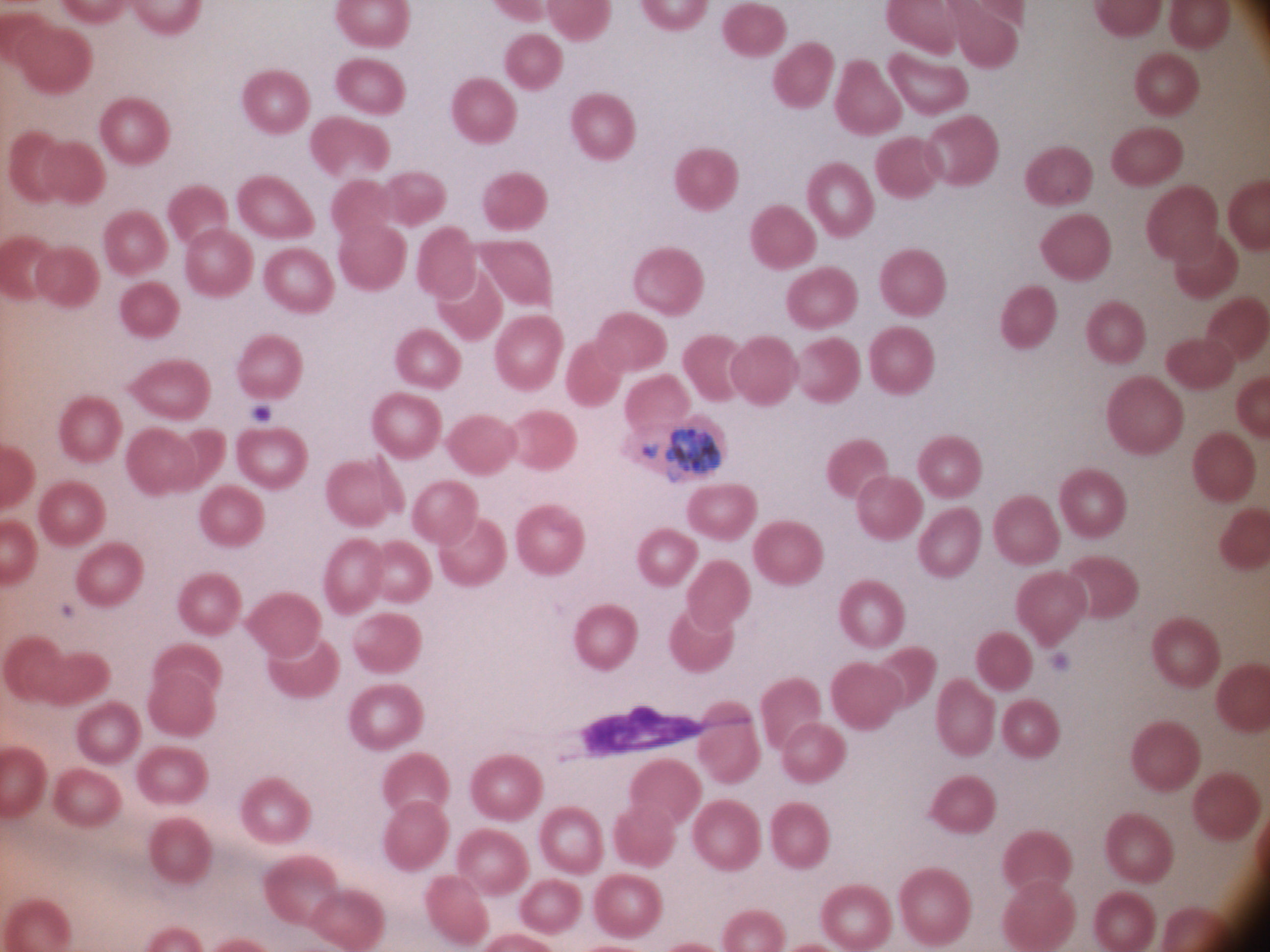

Approximate bounding boxes as [x1, y1, x2, y2] in pixels, from the source annotation, which is not necessarily exhaustive.
Summary:
  - Schizont locations: [665, 428, 721, 476]
  - Species: Plasmodium ovale
  - Image size: 1270×952 pixels
  - Field of view: one from this slide
  - Stain: Giemsa
  - Preparation: thin blood film
  - Microscope: Leica DM2000 with built-in camera
  - Magnification: 100x